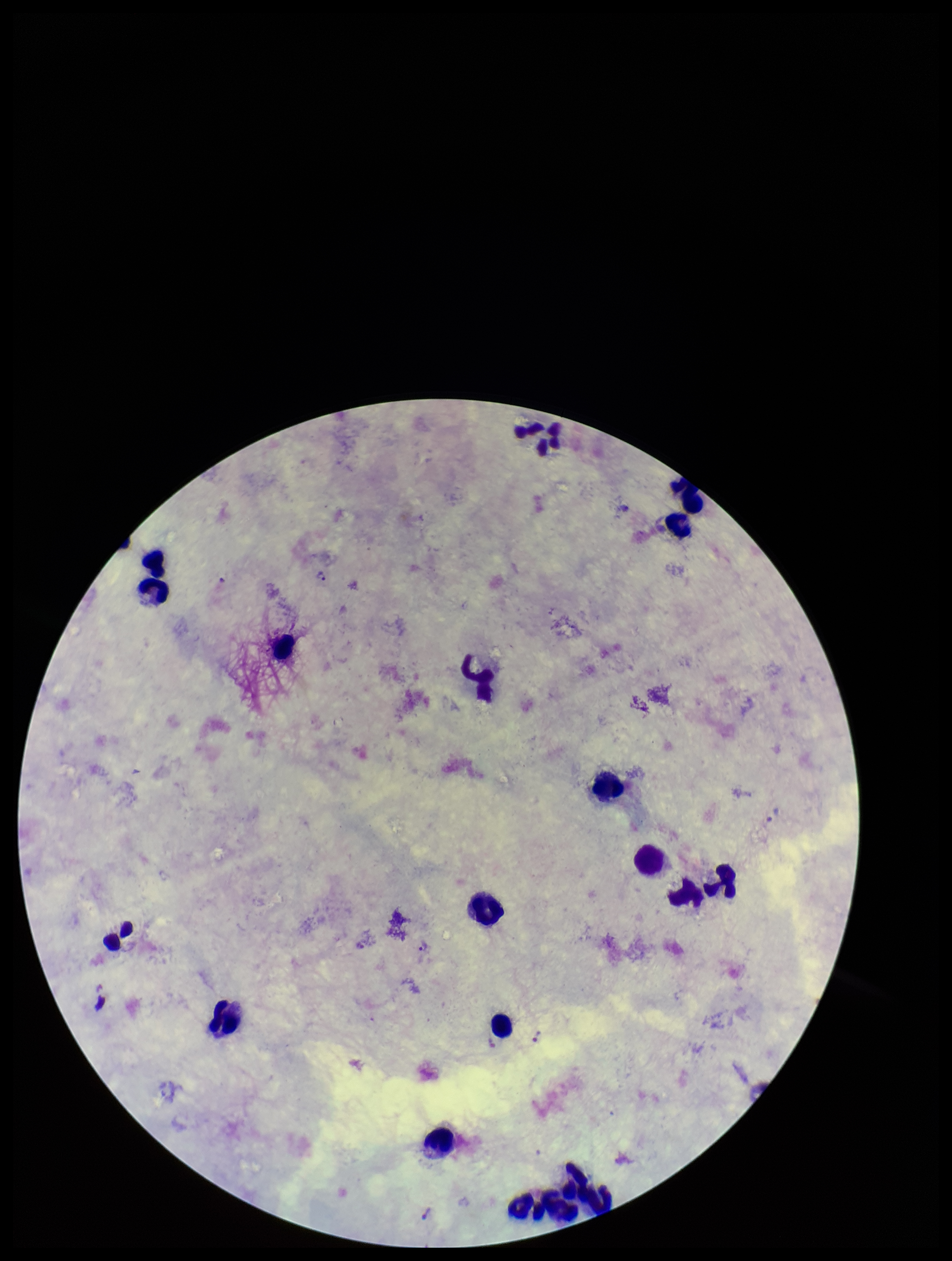

field_of_view: one from this slide
stain: Giemsa
parasite_count: 3
image_size: 952×1261 pixels
plasmodium_parasites: identified
patient_malaria_status: infected
preparation: thick
leukocyte_count: 17
species_reported_for_this_patient: Plasmodium vivax
capture: smartphone photograph through the microscope eyepiece